Outline each blood parasite and name the species.
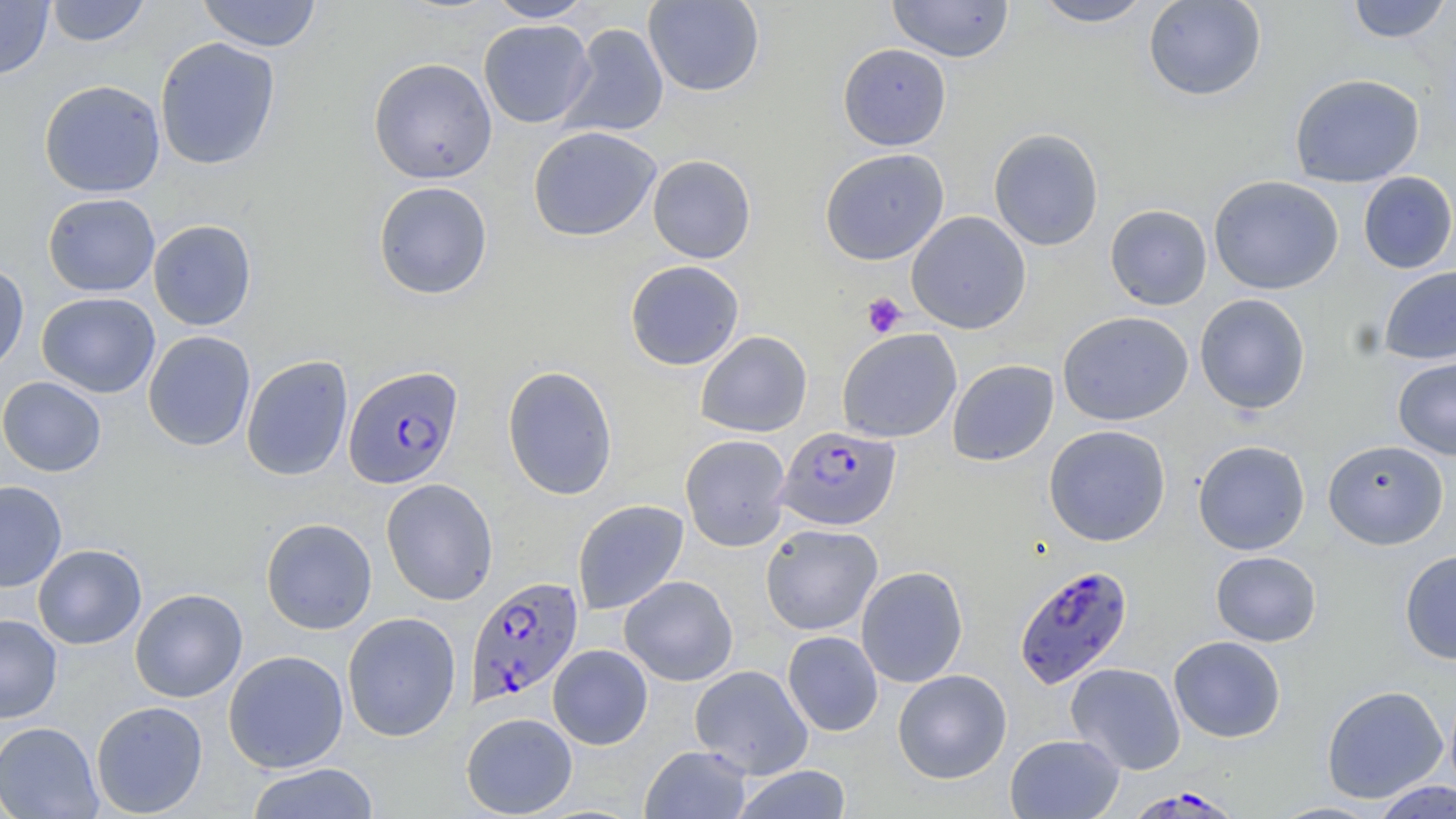
Approximate bounding boxes as (x1, y1, x2, y2) in pixels.
Plasmodium falciparum-infected red blood cells: (343, 365, 464, 488), (776, 425, 900, 531), (1013, 564, 1133, 688), (465, 576, 583, 707), (1131, 786, 1239, 818).
No Plasmodium ovale, Plasmodium malariae, Plasmodium vivax, Babesia divergens, or Trypanosoma brucei observed.

slide-level diagnosis = Plasmodium falciparum
uninfected red blood cell locations = approximate bounding boxes as (x1, y1, x2, y2) in pixels: (0, 0, 53, 79), (195, 0, 323, 52), (486, 0, 594, 22), (643, 0, 765, 97), (886, 0, 1015, 63), (1031, 0, 1154, 27), (1143, 0, 1267, 101), (1345, 0, 1453, 43), (45, 1, 150, 46), (478, 19, 595, 128), (558, 23, 669, 138), (155, 37, 281, 170), (838, 43, 951, 150), (368, 57, 497, 184), (1289, 73, 1425, 187), (39, 80, 166, 198), (528, 126, 661, 241), (988, 127, 1104, 251), (819, 148, 949, 265), (647, 154, 756, 263), (1357, 171, 1456, 274), (1208, 175, 1344, 295), (373, 180, 493, 300), (43, 193, 160, 297), (1105, 204, 1212, 310), (906, 211, 1031, 334), (148, 219, 257, 331), (625, 260, 744, 370), (0, 263, 30, 376), (1378, 265, 1456, 365), (36, 292, 161, 398), (1194, 294, 1311, 415), (1057, 311, 1193, 426), (836, 328, 962, 443), (696, 330, 812, 437), (143, 331, 256, 451), (241, 355, 354, 481), (1393, 357, 1456, 460), (947, 359, 1059, 466), (501, 365, 618, 500), (0, 376, 107, 477), (1043, 425, 1170, 546), (680, 434, 791, 551), (1323, 439, 1449, 550), (1193, 440, 1311, 555), (381, 478, 498, 605), (0, 480, 67, 592), (572, 499, 689, 615), (261, 517, 377, 634), (760, 523, 883, 635), (32, 544, 146, 650), (1399, 550, 1456, 664), (1210, 551, 1322, 646), (856, 565, 968, 687), (619, 575, 738, 686), (129, 588, 248, 703), (342, 611, 461, 741), (0, 614, 62, 723), (783, 631, 883, 736), (1169, 636, 1286, 743), (548, 644, 652, 749), (222, 650, 349, 773), (1066, 662, 1185, 775), (690, 664, 813, 779), (892, 669, 1012, 784), (1321, 685, 1448, 804), (91, 700, 208, 817), (461, 712, 577, 818), (0, 722, 103, 819), (1004, 734, 1124, 819), (640, 745, 753, 818), (246, 762, 379, 819), (731, 765, 853, 819), (1370, 780, 1456, 818), (1266, 801, 1386, 818)
field of view = one of a larger specimen
platelet locations = approximate bounding boxes as (x1, y1, x2, y2) in pixels: (862, 292, 907, 338)
preparation = thin blood smear
modality = light microscopy
magnification = 1000x
image size = 1456×819 pixels
stain = May-Grünwald-Giemsa